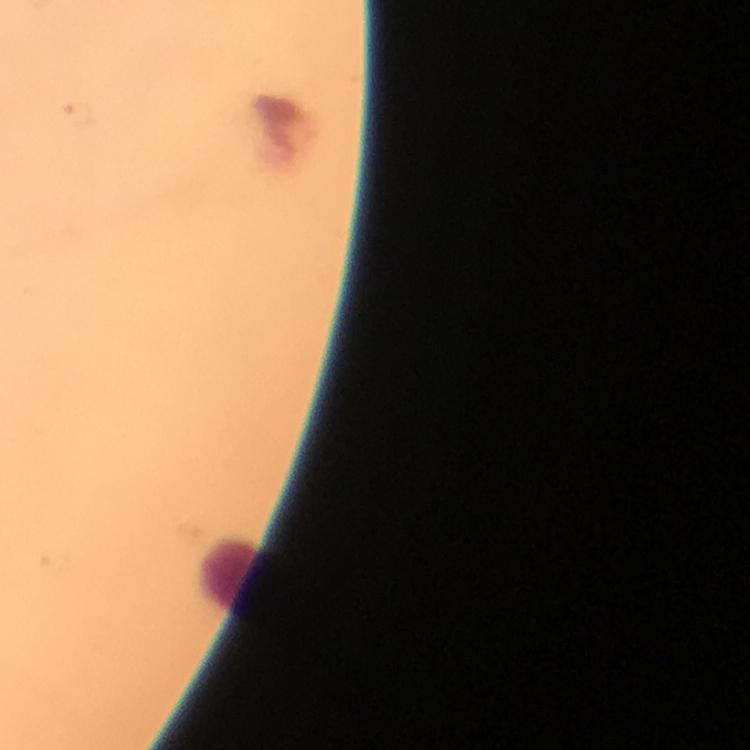
context = from a diagnostic examination for malaria
leukocyte locations = approximate centers as (x, y) in pixels: (228, 573)
stain = Giemsa
preparation = thick blood film
capture = smartphone camera through the microscope
immersion oil = applied
Plasmodium parasites = none detected
image size = 750×750 pixels
cropped from = a single field of view
magnification = 100x